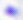

Toxoplasma gondii is seen. 400x magnification. Micrograph.